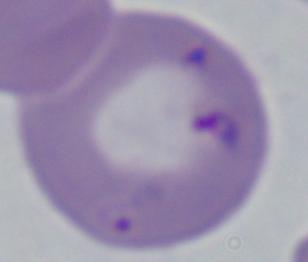
Summary:
  - Identification: Babesia
  - Modality: photomicrograph
  - Magnification: 1000x